Report the malaria status of this cell.
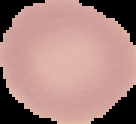

It is uninfected.

Image is 136×124 pixels. From a thin blood film. Cell region segmented out of the field of view; the surrounding area is masked to black.